Assess this cell for malaria.
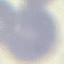
Uninfected.

{
  "stain": "Giemsa",
  "image_type": "automatically extracted cell patch, resized to 64 × 64 pixels",
  "capture": "smartphone camera at the microscope eyepiece",
  "preparation": "thin blood film"
}